Locate every Plasmodium falciparum-infected red blood cell.
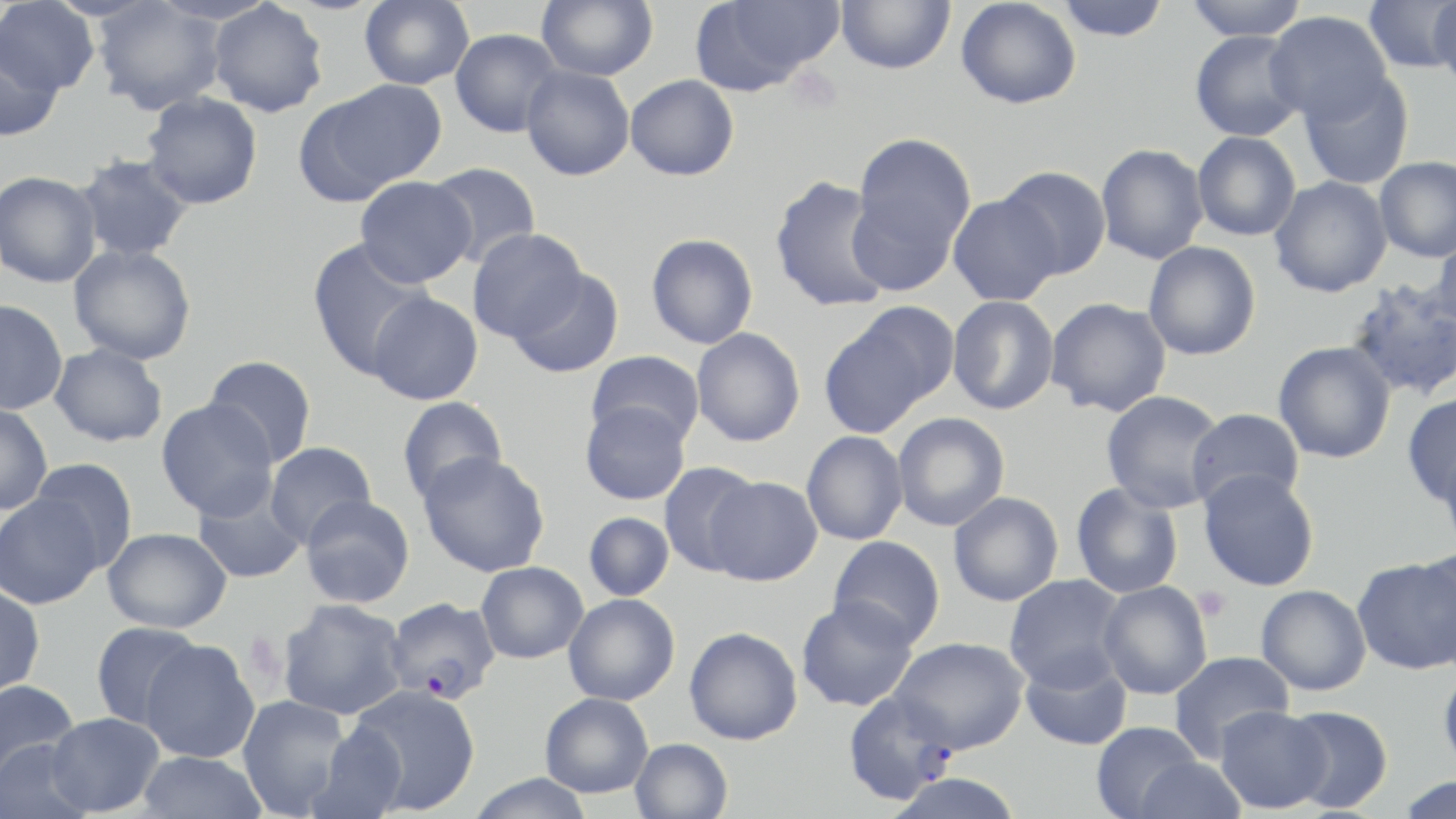

Approximate bounding boxes as named x1/y1/x2/y2 corners in pixels.
Plasmodium falciparum-infected red blood cells: (x1=386, y1=597, x2=500, y2=704), (x1=841, y1=692, x2=958, y2=806).

Summary:
  - Platelet locations: (x1=1195, y1=587, x2=1231, y2=621), (x1=242, y1=631, x2=289, y2=686)
  - Uninfected red blood cell locations: (x1=208, y1=0, x2=329, y2=118), (x1=359, y1=0, x2=474, y2=90), (x1=536, y1=0, x2=658, y2=81), (x1=835, y1=0, x2=955, y2=74), (x1=956, y1=0, x2=1082, y2=109), (x1=1056, y1=0, x2=1171, y2=42), (x1=1184, y1=0, x2=1308, y2=41), (x1=0, y1=1, x2=101, y2=97), (x1=91, y1=1, x2=227, y2=115), (x1=691, y1=1, x2=844, y2=94), (x1=1362, y1=1, x2=1456, y2=73), (x1=1430, y1=3, x2=1456, y2=96), (x1=1265, y1=11, x2=1392, y2=124), (x1=450, y1=28, x2=562, y2=137), (x1=1190, y1=30, x2=1306, y2=142), (x1=0, y1=38, x2=64, y2=142), (x1=521, y1=66, x2=635, y2=181), (x1=1298, y1=71, x2=1415, y2=190), (x1=625, y1=74, x2=739, y2=181), (x1=310, y1=80, x2=447, y2=197), (x1=142, y1=92, x2=263, y2=209), (x1=1192, y1=131, x2=1301, y2=241), (x1=853, y1=132, x2=976, y2=255), (x1=1095, y1=144, x2=1209, y2=265), (x1=74, y1=155, x2=195, y2=263), (x1=1373, y1=156, x2=1456, y2=262), (x1=426, y1=162, x2=541, y2=268), (x1=997, y1=166, x2=1112, y2=280), (x1=0, y1=171, x2=102, y2=288), (x1=355, y1=176, x2=476, y2=287), (x1=769, y1=176, x2=892, y2=313), (x1=1269, y1=176, x2=1393, y2=298), (x1=847, y1=191, x2=960, y2=295), (x1=947, y1=193, x2=1063, y2=306), (x1=467, y1=229, x2=587, y2=342), (x1=1429, y1=232, x2=1456, y2=335), (x1=646, y1=233, x2=758, y2=349), (x1=306, y1=238, x2=433, y2=379), (x1=1143, y1=241, x2=1261, y2=361), (x1=69, y1=245, x2=197, y2=365), (x1=508, y1=268, x2=624, y2=378), (x1=1344, y1=277, x2=1456, y2=401), (x1=367, y1=292, x2=483, y2=405), (x1=948, y1=295, x2=1059, y2=415), (x1=1045, y1=297, x2=1172, y2=417), (x1=0, y1=299, x2=68, y2=415), (x1=851, y1=301, x2=961, y2=406), (x1=818, y1=319, x2=932, y2=438), (x1=691, y1=328, x2=805, y2=447), (x1=1273, y1=341, x2=1396, y2=464), (x1=50, y1=343, x2=168, y2=447), (x1=586, y1=350, x2=705, y2=447), (x1=203, y1=355, x2=317, y2=467), (x1=1099, y1=391, x2=1229, y2=513), (x1=1401, y1=394, x2=1456, y2=506), (x1=396, y1=396, x2=508, y2=505), (x1=157, y1=399, x2=278, y2=521), (x1=580, y1=401, x2=691, y2=506), (x1=0, y1=403, x2=52, y2=515), (x1=1186, y1=407, x2=1304, y2=511), (x1=892, y1=412, x2=1010, y2=531), (x1=801, y1=431, x2=908, y2=545), (x1=265, y1=442, x2=377, y2=547), (x1=1438, y1=444, x2=1456, y2=556), (x1=417, y1=452, x2=551, y2=577), (x1=28, y1=458, x2=138, y2=571), (x1=658, y1=462, x2=763, y2=576), (x1=1198, y1=469, x2=1320, y2=592), (x1=705, y1=476, x2=823, y2=586), (x1=1071, y1=482, x2=1184, y2=599), (x1=193, y1=484, x2=306, y2=584), (x1=948, y1=492, x2=1064, y2=606), (x1=0, y1=493, x2=104, y2=609), (x1=300, y1=495, x2=415, y2=607), (x1=583, y1=511, x2=674, y2=601), (x1=103, y1=527, x2=231, y2=633), (x1=827, y1=535, x2=946, y2=648), (x1=1415, y1=544, x2=1456, y2=671), (x1=1352, y1=556, x2=1456, y2=674), (x1=476, y1=562, x2=588, y2=663), (x1=1004, y1=575, x2=1127, y2=690), (x1=1097, y1=581, x2=1212, y2=699), (x1=0, y1=584, x2=46, y2=698), (x1=1256, y1=584, x2=1372, y2=696), (x1=563, y1=594, x2=680, y2=706), (x1=796, y1=596, x2=919, y2=712), (x1=277, y1=599, x2=409, y2=720), (x1=90, y1=621, x2=204, y2=731), (x1=684, y1=626, x2=803, y2=745), (x1=890, y1=636, x2=1029, y2=753), (x1=140, y1=639, x2=260, y2=763), (x1=1019, y1=649, x2=1133, y2=751), (x1=1168, y1=650, x2=1294, y2=761), (x1=1438, y1=664, x2=1456, y2=777), (x1=0, y1=679, x2=80, y2=785), (x1=347, y1=684, x2=481, y2=815), (x1=540, y1=692, x2=653, y2=798), (x1=237, y1=695, x2=350, y2=817), (x1=1214, y1=705, x2=1332, y2=814), (x1=1282, y1=705, x2=1393, y2=813), (x1=45, y1=712, x2=165, y2=816), (x1=1091, y1=721, x2=1204, y2=819), (x1=306, y1=722, x2=408, y2=819), (x1=630, y1=738, x2=733, y2=819), (x1=1, y1=739, x2=97, y2=818), (x1=137, y1=751, x2=267, y2=819), (x1=1131, y1=757, x2=1246, y2=819), (x1=466, y1=773, x2=596, y2=819), (x1=884, y1=773, x2=1027, y2=819), (x1=1393, y1=775, x2=1456, y2=818)
  - Slide-level diagnosis: Plasmodium falciparum
  - Modality: optical microscopy
  - Magnification: 1000x
  - Preparation: thin blood smear
  - Image size: 1456×819 pixels
  - Stain: May-Grünwald-Giemsa
  - Field of view: single